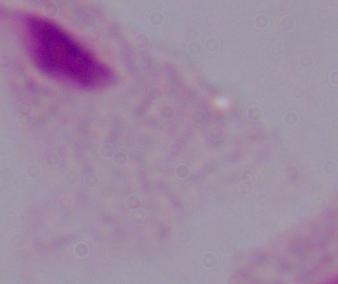
identification: trichomonad
modality: micrograph
magnification: 1000x